Classify this cell by malaria status.
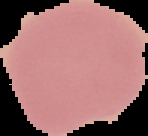
Uninfected.

Summary:
  - Image size: 148×136 pixels
  - Image type: segmented cell region on a black background
  - Preparation: thin blood smear